Name the parasite shown.
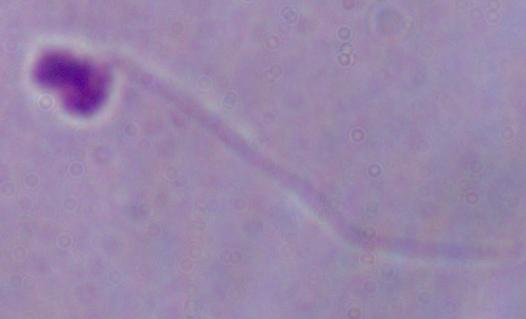
Leishmania.

magnification: 1000x
modality: micrograph